Classify this cell by malaria status.
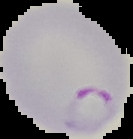
It is parasitized.

From a thin blood film. The area outside the segmented cell region is set to black. Image is 133×139 pixels.